Outline each Plasmodium falciparum-infected red blood cell.
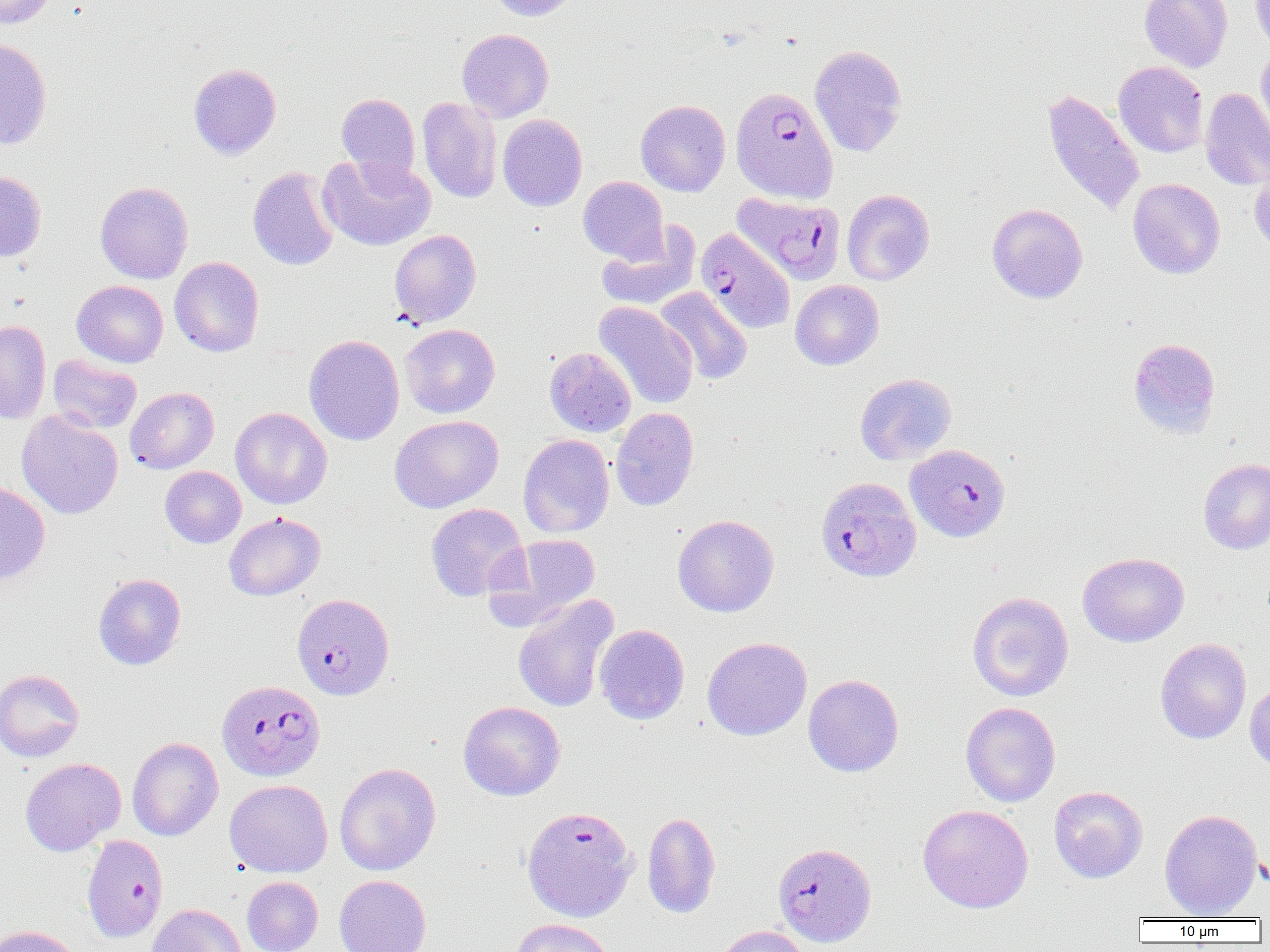
Approximate bounding boxes as (x1,y1)-(x2,y2) corner pairs in pixels.
Plasmodium falciparum-infected red blood cells: (731,86)-(838,203), (732,191)-(845,285), (695,228)-(795,333), (905,444)-(1010,542), (819,481)-(916,579), (292,593)-(395,700), (220,681)-(328,783), (521,805)-(637,922), (81,834)-(168,942), (773,841)-(876,947).

Summary:
  - Uninfected red blood cell locations: (1,0)-(57,29), (488,0)-(580,21), (1139,0)-(1232,72), (1250,0)-(1270,53), (457,28)-(554,122), (0,37)-(52,150), (809,44)-(907,157), (1256,44)-(1270,143), (1113,61)-(1209,158), (188,63)-(281,159), (1042,88)-(1145,218), (1200,88)-(1270,190), (337,93)-(420,182), (418,97)-(502,202), (635,100)-(730,196), (497,114)-(587,211), (317,154)-(436,251), (1249,162)-(1270,255), (248,166)-(340,271), (0,171)-(47,262), (578,176)-(668,263), (1127,178)-(1225,279), (95,181)-(193,283), (842,189)-(935,285), (986,203)-(1088,303), (597,225)-(700,312), (389,229)-(482,328), (169,256)-(264,357), (790,279)-(884,370), (72,280)-(168,367), (654,287)-(753,385), (594,301)-(698,409), (0,319)-(51,424), (400,324)-(500,418), (304,335)-(405,445), (1127,337)-(1221,439), (545,347)-(636,437), (47,354)-(142,434), (855,373)-(957,465), (125,386)-(218,474), (230,407)-(332,509), (610,407)-(699,511), (17,411)-(123,520), (389,415)-(504,513), (518,434)-(614,538), (1198,458)-(1270,554), (160,466)-(246,548), (0,481)-(50,582), (425,503)-(528,601), (224,511)-(325,600), (672,514)-(779,617), (488,533)-(601,626), (1078,552)-(1189,647), (93,573)-(186,670), (967,591)-(1074,702), (512,594)-(617,714), (594,624)-(690,725), (702,637)-(812,741), (1154,638)-(1251,744), (0,669)-(85,762), (803,674)-(904,777), (1244,681)-(1270,771), (457,701)-(565,801), (961,701)-(1061,807), (127,737)-(223,841), (20,758)-(126,856), (334,762)-(441,876), (224,779)-(333,877), (1049,785)-(1148,883), (918,804)-(1033,913), (1159,808)-(1263,919), (642,811)-(721,918), (334,874)-(431,952), (242,876)-(323,952), (146,904)-(247,952), (511,918)-(615,952), (1,925)-(80,952), (712,925)-(810,952)
  - Slide-level diagnosis: Plasmodium falciparum
  - Modality: optical microscopy
  - Preparation: thin blood smear
  - Magnification: 1000x
  - Field of view: single
  - Image size: 1270×952 pixels